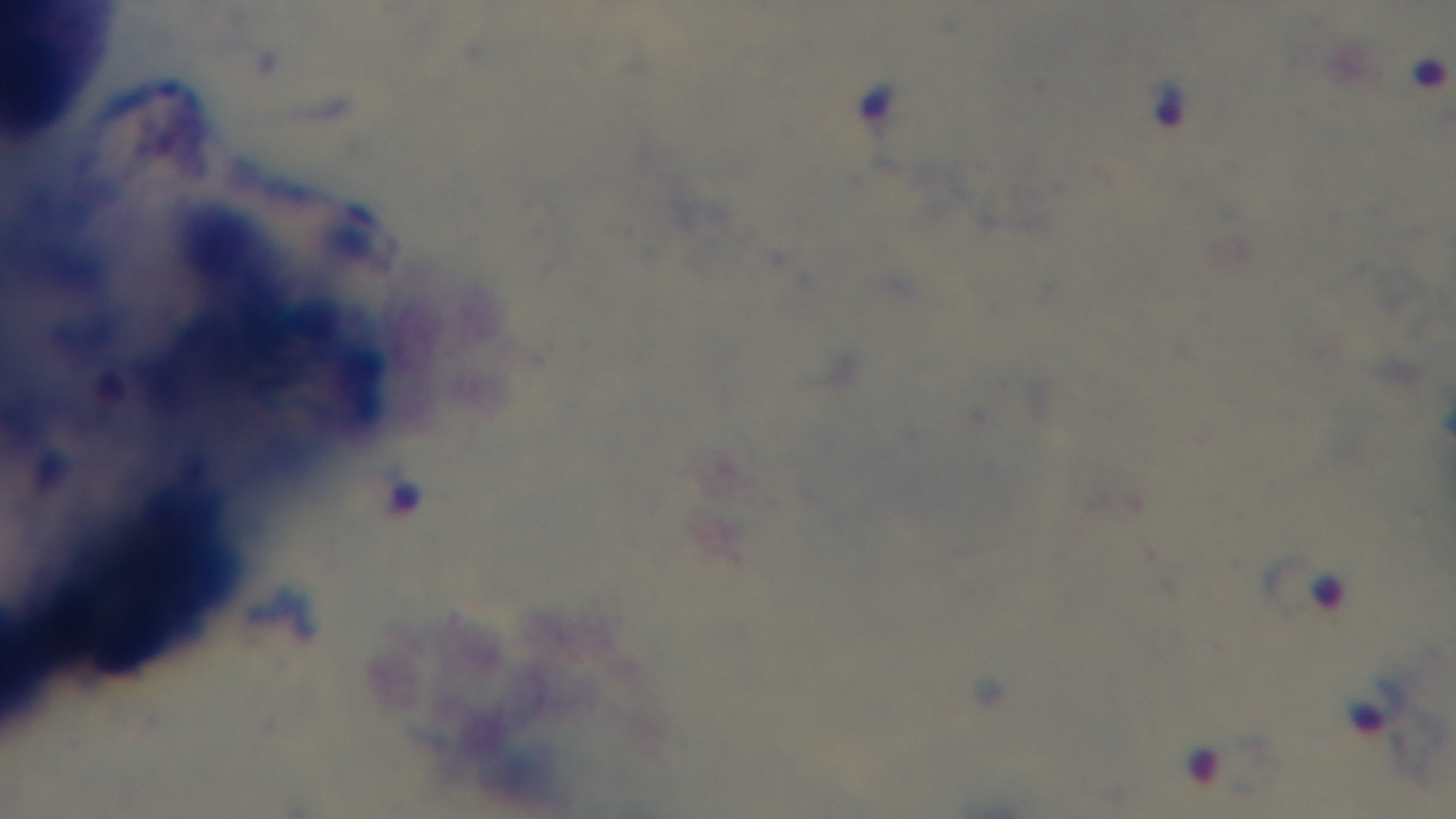

Malaria status: positive. Single field of view. Light microscopy. Preparation: thick blood film. Giemsa-stained. Mounted 4K digital camera. 100x oil-immersion objective.